Name the parasite shown.
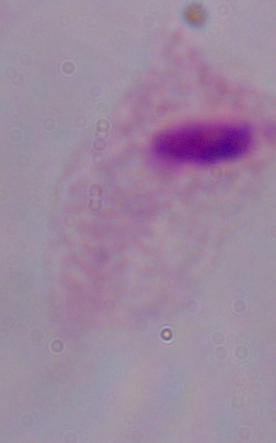
This is a trichomonad.

{
  "modality": "photomicrograph",
  "magnification": "1000x"
}